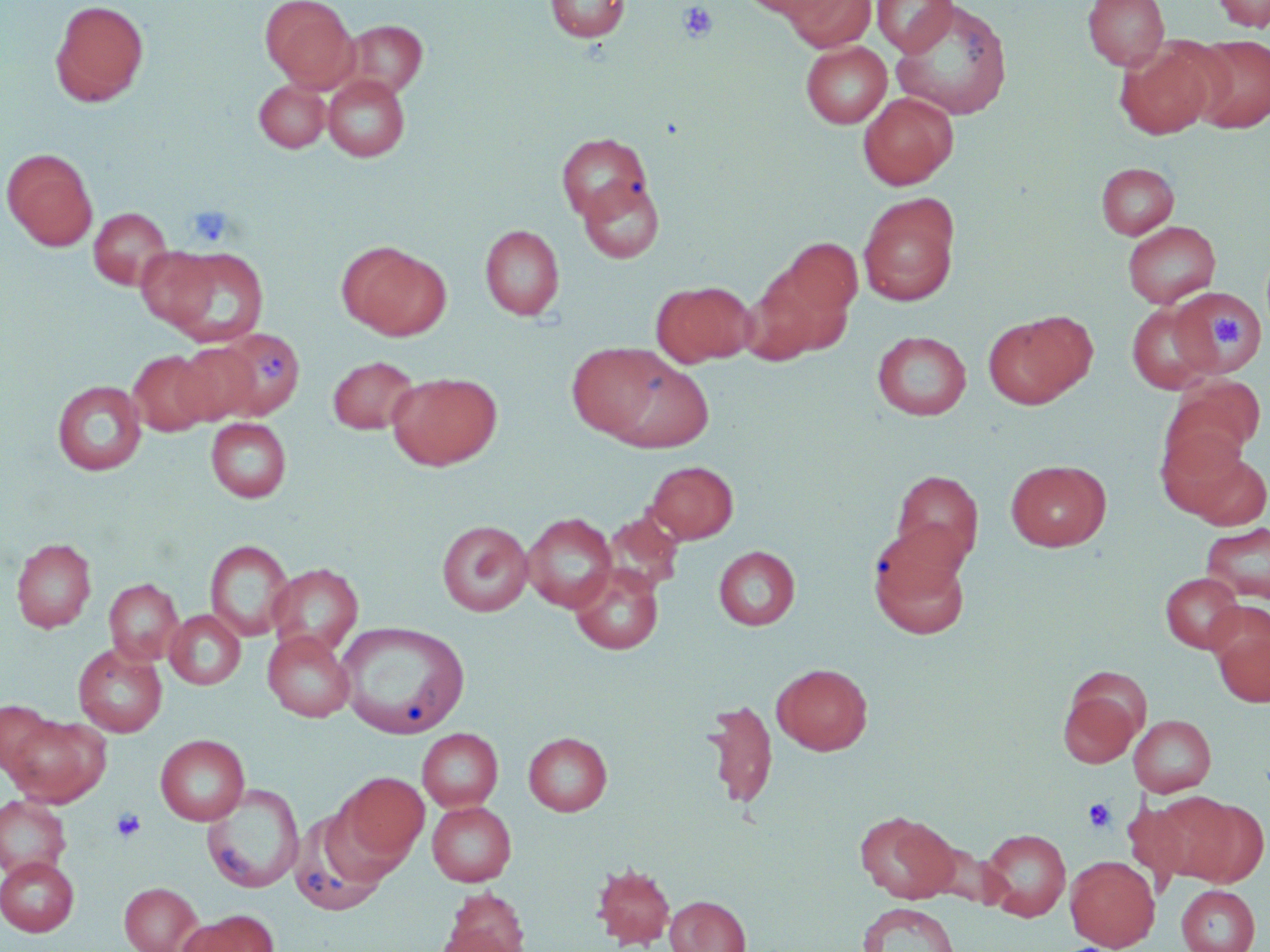
{
  "slide_level_diagnosis": "negative for blood parasites",
  "modality": "light microscopy",
  "stain": "May-Grünwald-Giemsa",
  "uninfected_red_blood_cell_locations": "approximate bounding boxes as [x1, y1, x2, y2] in pixels: [49, 0, 150, 108], [261, 0, 358, 91], [546, 0, 630, 42], [741, 0, 839, 20], [782, 0, 876, 51], [872, 0, 958, 56], [890, 0, 1014, 121], [1083, 0, 1169, 70], [1212, 0, 1270, 32], [342, 20, 428, 98], [1188, 34, 1270, 133], [800, 40, 892, 128], [1115, 42, 1219, 140], [323, 74, 410, 161], [253, 79, 330, 153], [858, 92, 959, 189], [556, 132, 653, 224], [2, 148, 98, 251], [1096, 162, 1179, 239], [578, 177, 665, 263], [858, 194, 960, 306], [88, 207, 173, 290], [1123, 221, 1221, 308], [480, 224, 565, 320], [341, 243, 450, 340], [135, 246, 222, 331], [748, 246, 856, 360], [161, 247, 270, 346], [652, 281, 754, 367], [1169, 288, 1266, 379], [1127, 303, 1216, 394], [983, 311, 1093, 409], [214, 327, 305, 418], [872, 330, 972, 420], [173, 341, 263, 424], [566, 343, 670, 440], [128, 350, 214, 436], [604, 355, 715, 453], [328, 356, 420, 434], [387, 372, 502, 470], [1162, 379, 1264, 472], [52, 380, 146, 476], [206, 417, 291, 502], [1173, 446, 1270, 530], [1005, 459, 1111, 551], [646, 460, 738, 543], [892, 470, 983, 570], [602, 511, 684, 595], [522, 513, 618, 612], [437, 520, 533, 616], [1201, 521, 1270, 606], [868, 527, 971, 635], [11, 538, 96, 633], [205, 539, 294, 641], [714, 546, 800, 629], [267, 563, 364, 656], [570, 565, 663, 655], [1161, 572, 1245, 653], [104, 578, 184, 665], [1209, 608, 1270, 708], [165, 610, 245, 689], [337, 621, 470, 739], [262, 631, 355, 722], [73, 643, 167, 737], [773, 663, 872, 755], [1059, 685, 1144, 768], [703, 699, 778, 810], [0, 700, 60, 777], [4, 712, 111, 807], [1128, 714, 1217, 797], [418, 728, 503, 811], [523, 732, 612, 816], [155, 734, 249, 825], [339, 772, 429, 861], [203, 785, 304, 893], [0, 794, 72, 880], [1159, 794, 1265, 887], [427, 801, 516, 886], [289, 809, 392, 917], [854, 810, 960, 903], [980, 828, 1071, 921], [0, 856, 78, 936], [1065, 856, 1159, 951], [591, 863, 675, 949], [119, 882, 204, 952], [1176, 885, 1260, 952], [443, 886, 529, 952], [665, 896, 751, 952], [858, 903, 959, 952], [180, 910, 278, 952], [431, 926, 521, 952]",
  "image_size": "1270×952 pixels",
  "field_of_view": "single",
  "platelet_locations": "approximate bounding boxes as [x1, y1, x2, y2] in pixels: [678, 2, 718, 43], [187, 205, 234, 246], [1214, 313, 1243, 348], [258, 352, 288, 385], [1083, 798, 1116, 833], [111, 807, 146, 842]",
  "magnification": "1000x",
  "preparation": "thin blood film"
}